Comment on the morphology of the erythrocytes.
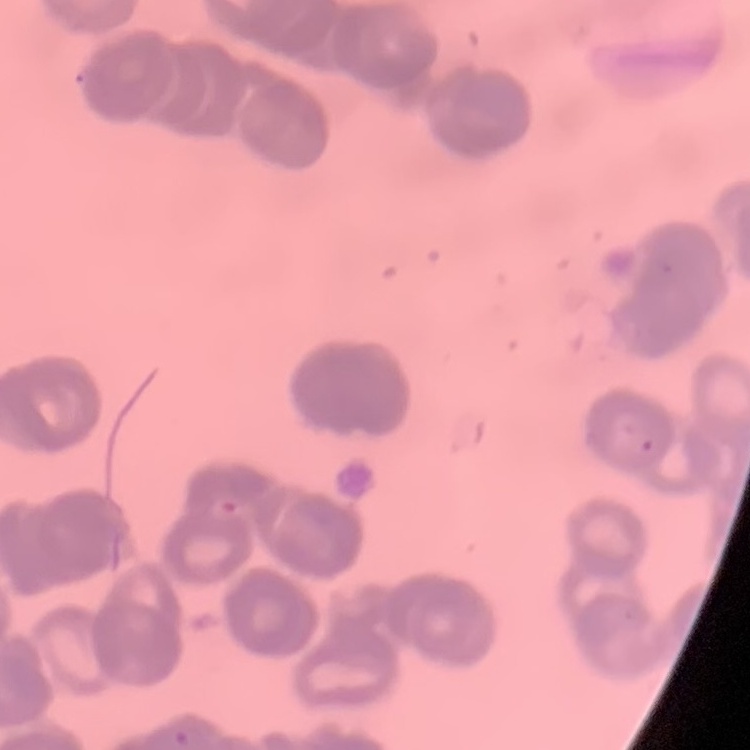

They show rouleaux formation.

preparation = thin peripheral smear
stain = Field's or Giemsa
image type = square crop of a larger photomicrograph